Assess the morphology of the red blood cells.
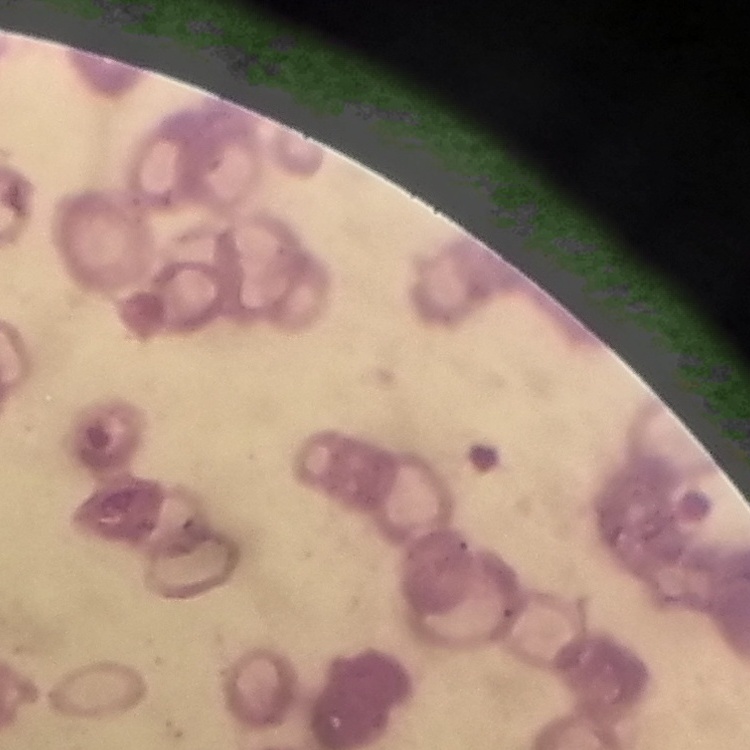

Rouleaux formation.

{
  "preparation": "thin peripheral smear",
  "image_type": "square crop of a larger photomicrograph",
  "stain": "Field's or Giemsa"
}